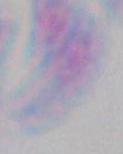

magnification = 1000x
identification = Toxoplasma gondii
modality = micrograph